Assess this cell for malaria.
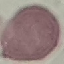

It is uninfected.

Summary:
  - Preparation: thin blood smear
  - Stain: Giemsa
  - Image type: cell patch, automatically extracted from a larger field of view and resized to 64 × 64 pixels
  - Capture: smartphone camera at the microscope eyepiece